Report the malaria status of this cell.
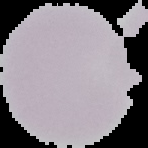
It is uninfected.

Summary:
  - Image size: 148×148 pixels
  - Image type: cell region segmented out of the field of view; surrounding area masked to black
  - Preparation: thin blood film